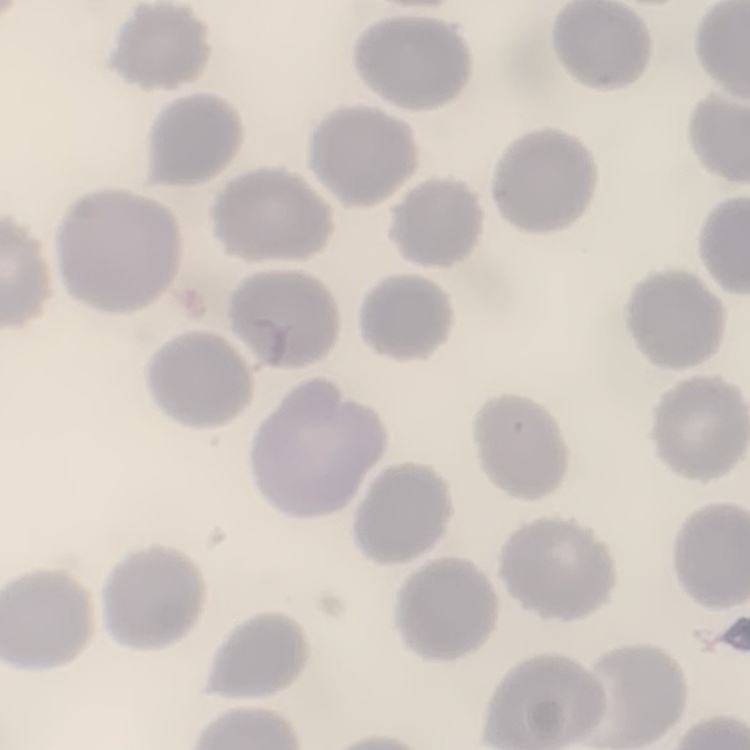
The red blood cells show no rouleaux formation. Thin blood film. Field's or Giemsa stain. One tile cut from a larger photomicrograph.